Classify this cell by malaria status.
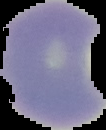
It is parasitized.

The area outside the segmented cell region is set to black. From a thin blood film. Image is 106×130 pixels.